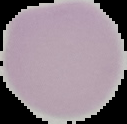

{
  "image_type": "cell region segmented out of the field of view; surrounding area masked to black",
  "image_size": "127×124 pixels",
  "result": "no Plasmodium parasites detected",
  "preparation": "thin blood film"
}